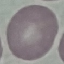

{
  "malaria_status": "uninfected",
  "stain": "Giemsa",
  "capture": "smartphone through the microscope eyepiece",
  "preparation": "thin smear",
  "image_type": "automatically extracted cell patch, resized to 64 × 64 pixels"
}